Classify this cell by malaria status.
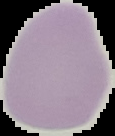

It is uninfected.

preparation = thin blood film
image type = segmented cell region on a black background
image size = 115×136 pixels